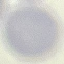

result: negative for malaria parasites
preparation: thin smear
stain: Giemsa
image_type: cell patch, automatically extracted from a larger field of view and resized to 64 × 64 pixels
capture: smartphone camera at the microscope eyepiece